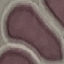
result: no malaria parasites detected
stain: Giemsa
image_type: cell patch, automatically extracted from a larger field of view and resized to 64 × 64 pixels
preparation: thin blood film
capture: smartphone camera at the microscope eyepiece